Outline each blood parasite and name the species.
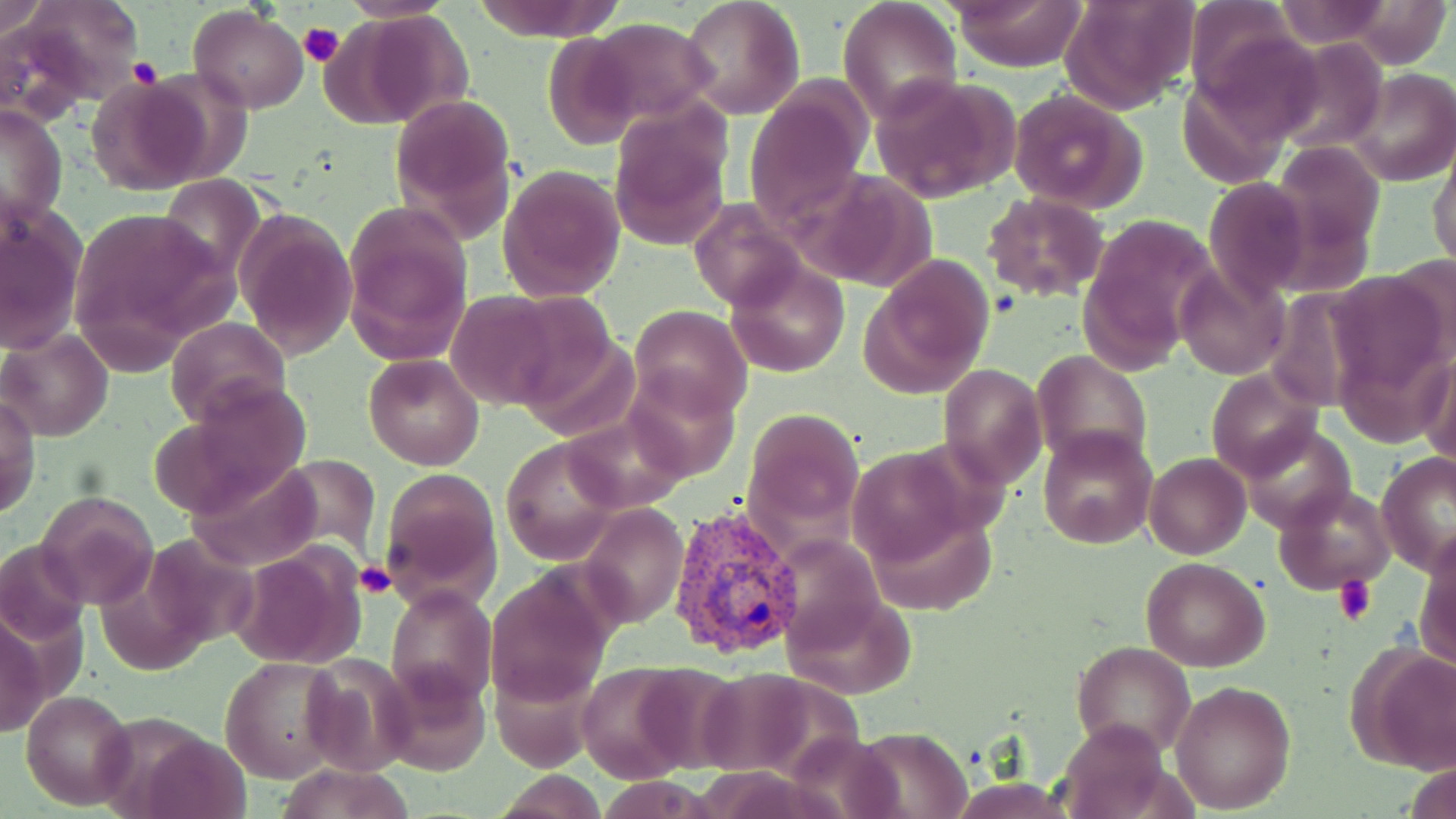

Approximate bounding boxes as [x1, y1, x2, y2] in pixels.
Plasmodium vivax-infected red blood cells: [665, 502, 804, 660].
No Plasmodium falciparum, Plasmodium ovale, Plasmodium malariae, Babesia divergens, or Trypanosoma brucei observed.

Platelet locations: [299, 19, 345, 69], [129, 58, 161, 87], [357, 561, 397, 599], [1333, 576, 1376, 625]. Uninfected red blood cell locations: [2, 0, 51, 43], [9, 0, 141, 108], [472, 0, 626, 41], [680, 0, 805, 119], [948, 0, 1086, 71], [1059, 0, 1199, 114], [1185, 0, 1306, 109], [837, 1, 963, 121], [1266, 1, 1401, 50], [189, 6, 309, 112], [331, 12, 473, 129], [586, 19, 715, 125], [543, 33, 643, 147], [1274, 38, 1386, 156], [1345, 67, 1453, 186], [85, 74, 211, 195], [871, 74, 1023, 202], [1007, 88, 1148, 214], [744, 91, 868, 231], [390, 93, 517, 235], [1, 104, 68, 227], [609, 112, 732, 252], [1273, 139, 1384, 256], [1430, 140, 1456, 274], [496, 164, 625, 303], [159, 175, 266, 280], [1205, 178, 1312, 303], [980, 195, 1111, 302], [691, 197, 808, 310], [1, 203, 88, 354], [64, 204, 236, 366], [344, 205, 474, 362], [235, 209, 359, 361], [862, 254, 993, 397], [725, 259, 850, 378], [1172, 265, 1289, 381], [445, 291, 572, 409], [628, 304, 750, 420], [165, 316, 290, 429], [0, 329, 113, 441], [1033, 351, 1153, 470], [1418, 352, 1455, 471], [363, 355, 484, 469], [938, 363, 1045, 489], [620, 365, 744, 485], [1205, 370, 1320, 481], [156, 378, 314, 522], [1, 395, 40, 518], [743, 407, 864, 531], [559, 411, 693, 513], [1244, 425, 1357, 534], [1037, 427, 1158, 550], [499, 437, 625, 564], [1144, 453, 1250, 560], [1376, 453, 1454, 575], [385, 471, 502, 605], [1274, 483, 1398, 594], [36, 491, 159, 610], [579, 502, 687, 629], [1415, 533, 1456, 672], [0, 541, 88, 645], [230, 544, 370, 670], [1143, 556, 1269, 672], [482, 566, 617, 709], [385, 583, 497, 706], [0, 611, 44, 741], [1073, 640, 1197, 756], [1348, 644, 1456, 776], [298, 653, 418, 775], [221, 655, 346, 783], [375, 661, 491, 776], [573, 663, 697, 780], [1169, 680, 1295, 813], [22, 688, 136, 810], [97, 715, 233, 813], [1058, 717, 1172, 819], [274, 763, 418, 819], [494, 772, 607, 818]. Slide-level diagnosis: Plasmodium vivax. Optical microscopy. May-Grünwald-Giemsa-stained preparation. Captured at 1000x magnification. Image is 1456×819 pixels. Thin blood smear. One field of a larger specimen.